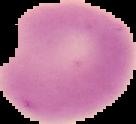

Summary:
  - Preparation: thin blood film
  - Image type: segmented cell region with the area outside set to black
  - Image size: 136×124 pixels
  - Result: no malaria parasites seen